Comment on the morphology of the erythrocytes.
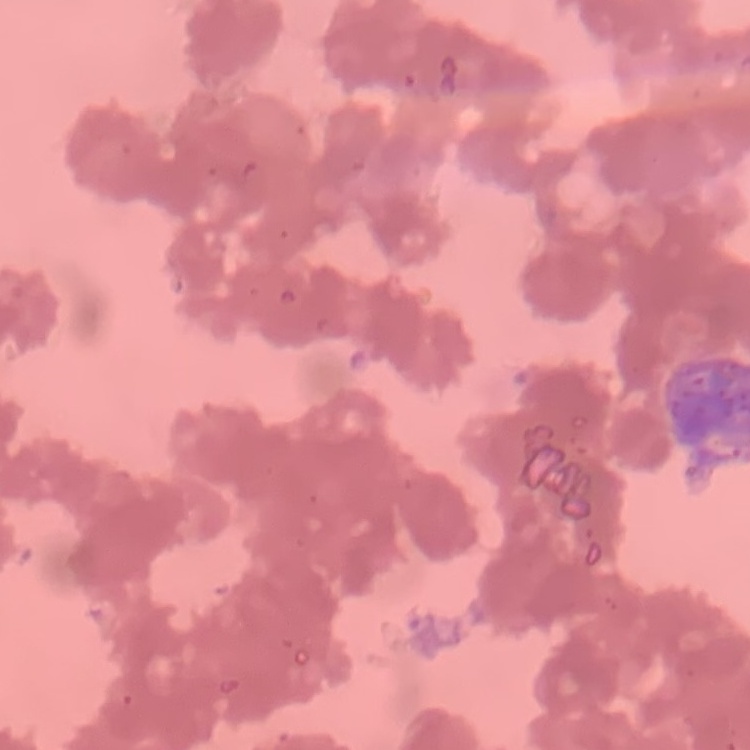

Rouleaux formation.

stain = Field's or Giemsa
preparation = thin blood smear
image type = one tile cut from a larger photomicrograph